Name the cell type shown.
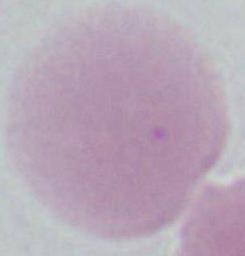

This is an erythrocyte.

Photomicrograph. Captured at 1000x magnification.